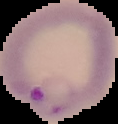

Summary:
  - Preparation: thin blood smear
  - Image size: 118×124 pixels
  - Malaria status: parasitized
  - Image type: segmented cell region on a black background